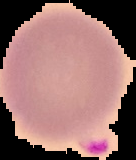

preparation = thin blood smear
image size = 136×160 pixels
image type = cell region segmented out of the field of view; surrounding area masked to black
result = Plasmodium parasites identified